Locate every Trypanosoma brucei.
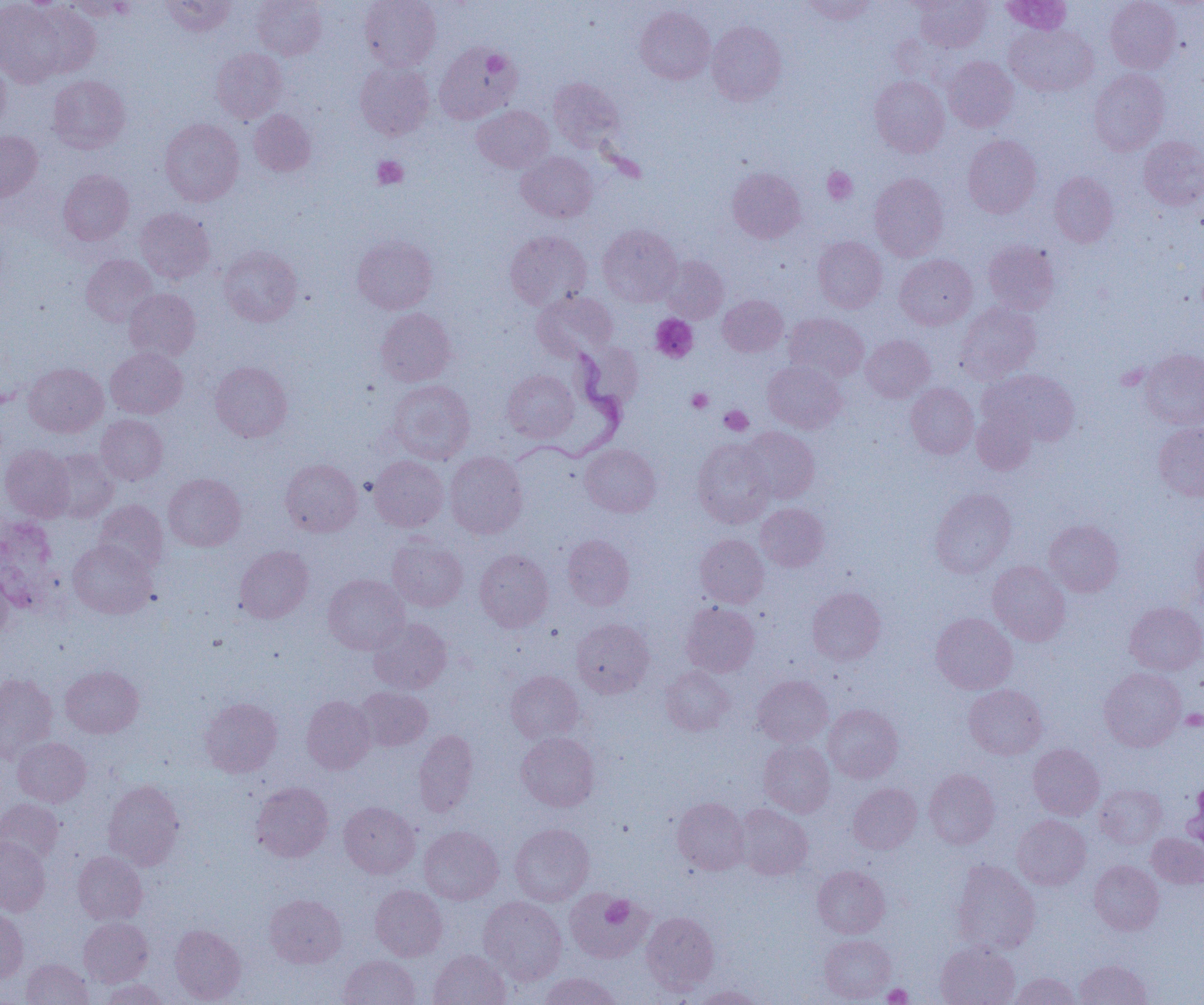
Approximate bounding boxes as (x1,y1)-(x2,y2) corner pairs in pixels.
Trypanosoma brucei: (516,340)-(629,462).

Summary:
  - Platelet locations: (372,155)-(408,189), (822,167)-(857,205), (651,314)-(698,363), (687,388)-(713,413), (719,405)-(753,436), (1182,709)-(1204,730), (601,895)-(634,926), (882,983)-(913,1005)
  - Uninfected red blood cell locations: (64,0)-(136,20), (161,0)-(236,37), (252,0)-(326,60), (360,0)-(441,71), (800,0)-(878,25), (1000,0)-(1072,34), (1105,0)-(1181,74), (0,1)-(67,87), (915,1)-(992,51), (29,2)-(102,78), (635,6)-(715,84), (707,21)-(787,106), (1005,23)-(1097,96), (434,42)-(521,124), (211,48)-(287,123), (945,56)-(1018,132), (0,59)-(10,133), (355,61)-(434,140), (1089,69)-(1169,155), (48,75)-(130,153), (870,75)-(949,157), (548,77)-(624,152), (472,105)-(553,173), (249,110)-(316,176), (160,118)-(244,206), (0,131)-(42,201), (963,134)-(1042,218), (1138,136)-(1204,210), (517,151)-(597,223), (727,167)-(806,243), (59,169)-(134,245), (1050,171)-(1118,247), (869,173)-(949,261), (135,207)-(215,283), (598,224)-(682,306), (504,230)-(592,309), (352,235)-(437,314), (813,236)-(887,312), (983,239)-(1060,314), (219,245)-(302,326), (81,254)-(157,326), (894,254)-(977,329), (660,255)-(729,323), (124,288)-(200,361), (532,291)-(618,362), (718,295)-(788,356), (955,302)-(1041,384), (375,308)-(456,386), (784,313)-(869,382), (861,335)-(935,402), (106,347)-(187,419), (1139,348)-(1204,429), (210,361)-(293,442), (763,361)-(847,434), (24,363)-(108,437), (983,368)-(1079,446), (503,370)-(578,442), (387,379)-(475,463), (906,383)-(978,458), (972,404)-(1038,475), (96,415)-(167,484), (1153,423)-(1204,501), (740,426)-(820,503), (692,439)-(775,528), (1,444)-(75,522), (580,444)-(661,517), (46,448)-(119,522), (444,451)-(528,538), (369,456)-(448,531), (281,458)-(362,536), (163,473)-(245,550), (929,487)-(1016,578), (94,500)-(168,574), (756,503)-(829,572), (1043,519)-(1123,596), (1190,533)-(1204,615), (562,534)-(634,610), (695,534)-(768,607), (387,535)-(468,611), (68,539)-(157,618), (234,546)-(313,623), (475,549)-(554,632), (987,561)-(1071,646), (0,567)-(13,640), (323,574)-(409,654), (807,587)-(886,665), (680,602)-(760,676), (1125,602)-(1204,675), (931,612)-(1017,694), (368,618)-(452,694), (571,619)-(654,697), (60,666)-(143,737), (661,666)-(734,735), (1099,667)-(1186,751), (506,670)-(583,743), (0,673)-(57,763), (753,675)-(833,747), (963,684)-(1047,760), (355,686)-(432,751), (301,696)-(375,773), (200,698)-(282,777), (823,704)-(903,783), (414,730)-(478,816), (516,732)-(599,811), (13,737)-(91,807), (759,740)-(835,817), (1028,743)-(1104,820), (924,769)-(1000,849), (102,779)-(185,870), (251,782)-(333,862), (848,783)-(922,854), (1094,784)-(1167,848), (672,797)-(750,874), (0,799)-(63,866), (339,801)-(420,879), (735,804)-(813,879), (1012,814)-(1091,890), (510,823)-(594,906), (419,826)-(503,904), (1146,833)-(1204,888), (0,837)-(50,916), (73,851)-(147,925), (952,860)-(1041,954), (1089,860)-(1164,935), (813,865)-(890,938), (370,885)-(447,961), (565,889)-(653,963), (264,893)-(346,968), (478,896)-(567,984), (0,908)-(28,983), (641,911)-(719,992), (79,917)-(153,986), (170,924)-(246,1004), (819,934)-(896,1003), (935,941)-(1020,1005), (428,949)-(511,1005), (339,955)-(420,1005), (21,958)-(93,1005), (1074,959)-(1151,1005), (539,972)-(623,1005), (1011,972)-(1081,1005), (101,978)-(168,1005), (692,986)-(764,1004)
  - Slide-level diagnosis: Trypanosoma brucei
  - Modality: optical microscopy
  - Magnification: 1000x
  - Field of view: one of a larger specimen
  - Preparation: thin blood smear
  - Image size: 1204×1005 pixels